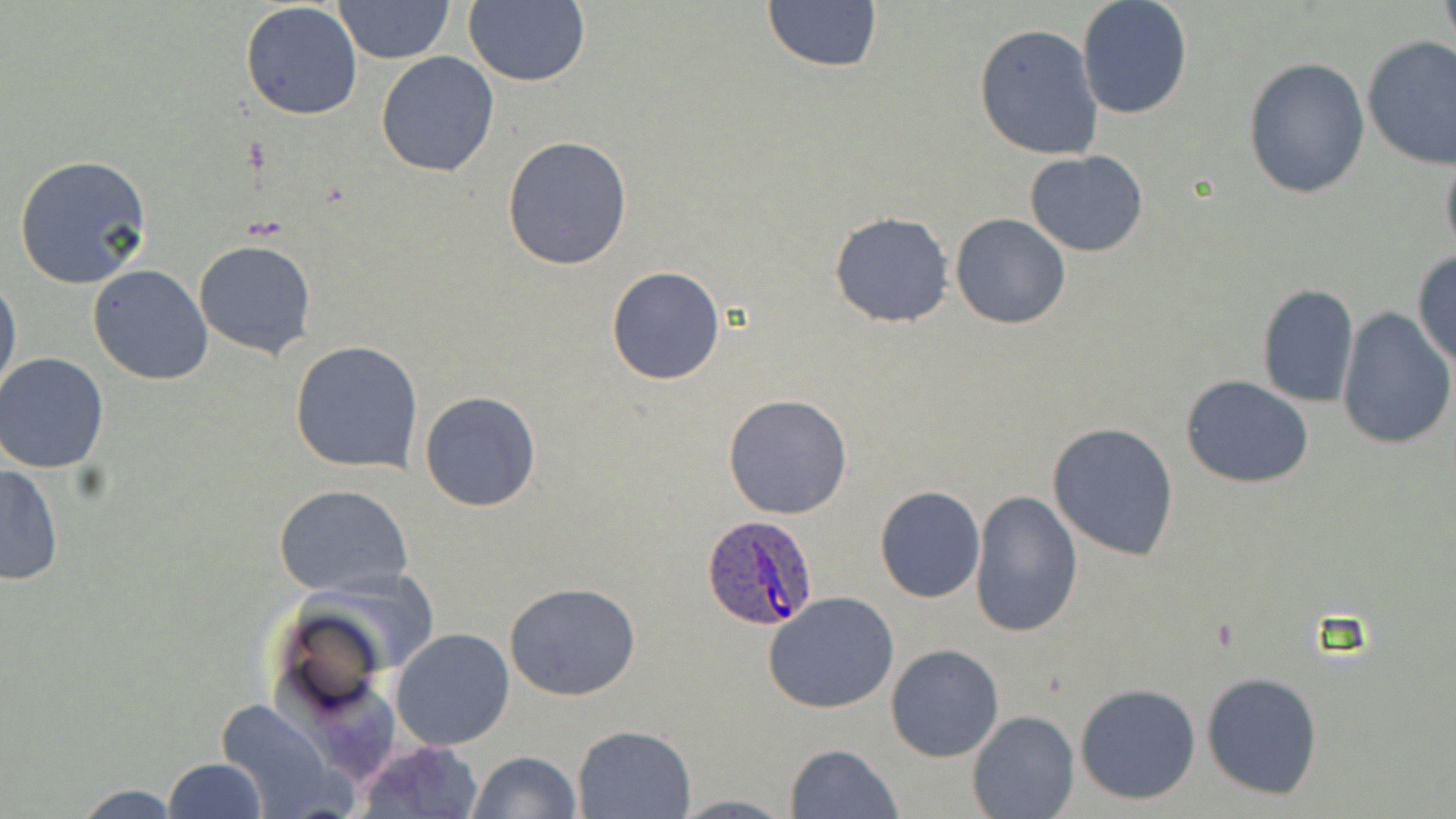
Summary:
  - Coordinate format: approximate bounding boxes as [x1, y1, x2, y2] in pixels
  - Uninfected red blood cell locations: [333, 0, 455, 66], [1077, 0, 1193, 120], [1438, 0, 1455, 47], [762, 1, 882, 72], [462, 2, 590, 87], [240, 3, 363, 119], [974, 23, 1104, 161], [1361, 35, 1456, 170], [374, 50, 501, 178], [1242, 57, 1369, 198], [503, 135, 634, 270], [1440, 149, 1456, 263], [1025, 152, 1150, 255], [14, 155, 154, 289], [829, 211, 953, 327], [950, 213, 1070, 330], [192, 240, 317, 359], [1411, 251, 1456, 365], [88, 264, 214, 385], [607, 266, 726, 385], [1, 271, 20, 400], [1256, 284, 1359, 408], [1252, 291, 1456, 421], [1338, 309, 1455, 449], [290, 340, 422, 473], [0, 352, 109, 473], [1180, 375, 1315, 489], [419, 390, 542, 512], [723, 393, 855, 520], [1048, 422, 1180, 562], [0, 462, 65, 587], [274, 484, 414, 597], [874, 486, 986, 603], [970, 490, 1082, 636], [504, 581, 642, 700], [763, 592, 899, 714], [391, 628, 514, 750], [885, 643, 1005, 763], [1201, 672, 1322, 798], [1075, 682, 1201, 805], [212, 699, 346, 819], [968, 710, 1079, 819], [571, 725, 696, 817], [353, 740, 484, 819], [785, 742, 903, 819], [466, 751, 581, 819], [161, 757, 269, 819], [65, 783, 189, 817], [673, 794, 795, 818]
  - Plasmodium ovale-infected red blood cell locations: [700, 512, 820, 632]
  - Slide-level diagnosis: Plasmodium ovale
  - Modality: light microscopy
  - Field of view: one of a larger specimen
  - Image size: 1456×819 pixels
  - Preparation: thin blood film
  - Stain: May-Grünwald-Giemsa
  - Magnification: 1000x